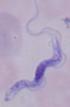
Photomicrograph. A trypanosome is seen. Captured at 1000x magnification.